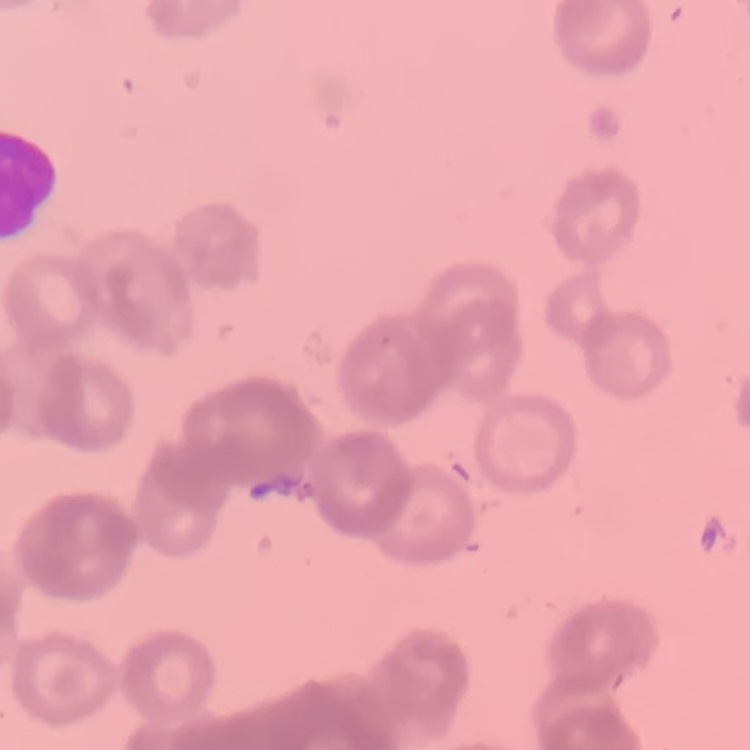

red_blood_cell_morphology: rouleaux formation
stain: Field's or Giemsa
image_type: square crop of a larger photomicrograph
preparation: thin blood film